Assess this cell for malaria.
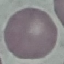

It is uninfected.

Photographed with a smartphone camera at the microscope eyepiece. Giemsa-stained preparation. Thin blood smear. Cell patch, automatically extracted from a larger field of view and resized to 64 × 64 pixels.